Give the extent of all Plasmodium vivax-infected red blood cells.
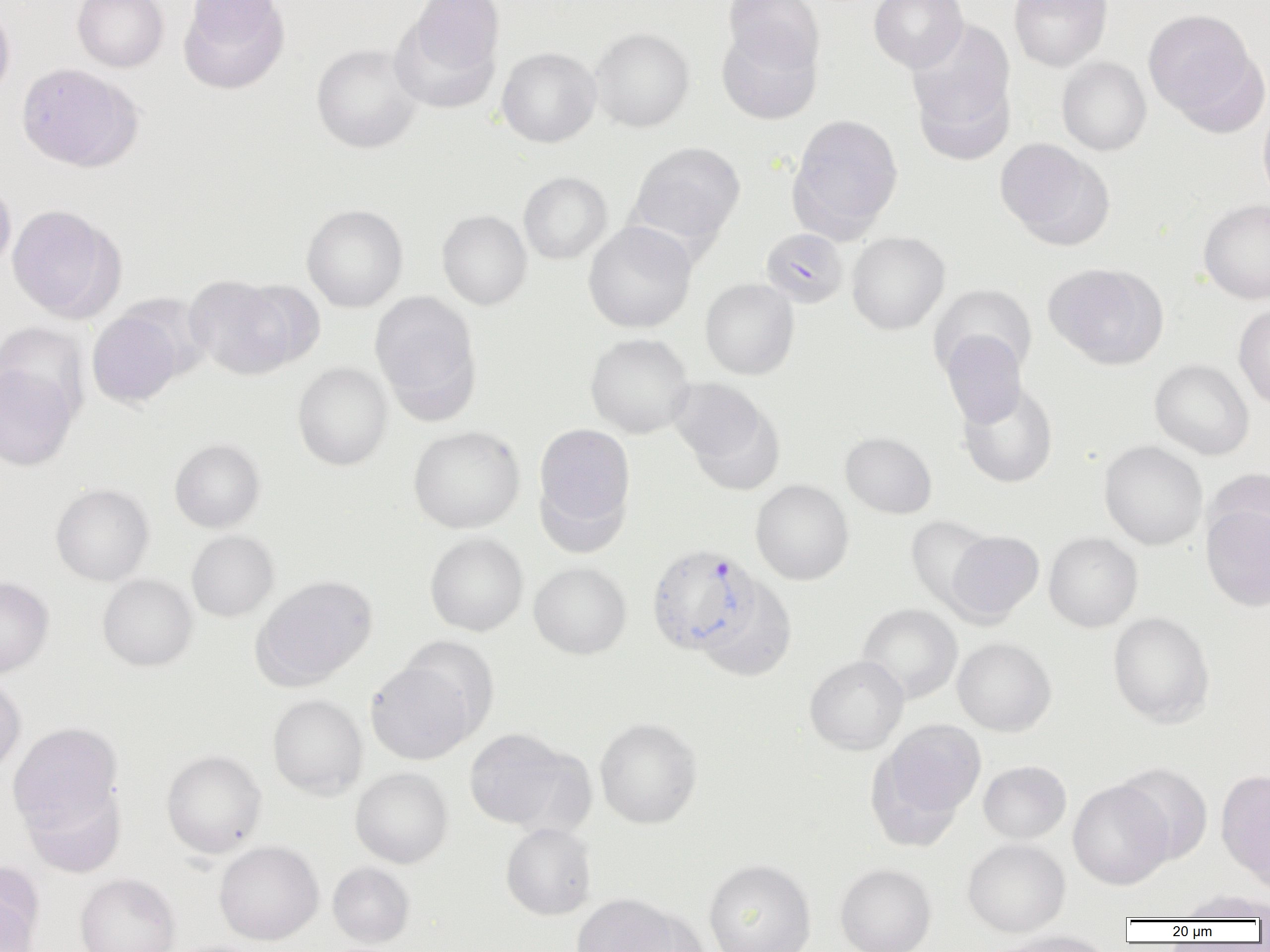

Approximate bounding boxes as [x1, y1, x2, y2] in pixels.
Plasmodium vivax-infected red blood cells: [646, 544, 761, 655].

Summary:
  - Uninfected red blood cell locations: [72, 0, 169, 72], [178, 0, 289, 93], [395, 0, 505, 95], [722, 0, 823, 72], [868, 0, 967, 72], [1009, 0, 1112, 71], [0, 3, 16, 102], [1143, 10, 1259, 124], [906, 20, 1016, 154], [716, 25, 823, 125], [591, 27, 694, 132], [311, 43, 423, 153], [496, 46, 602, 147], [1057, 57, 1152, 156], [16, 63, 141, 171], [1258, 104, 1270, 207], [788, 113, 903, 239], [995, 138, 1111, 247], [627, 141, 745, 250], [518, 171, 612, 264], [0, 180, 16, 276], [1198, 199, 1270, 304], [302, 204, 408, 312], [7, 205, 122, 321], [437, 209, 532, 310], [583, 221, 697, 333], [761, 227, 849, 308], [846, 231, 950, 335], [1043, 262, 1168, 369], [185, 274, 298, 380], [237, 278, 325, 369], [700, 278, 799, 380], [929, 284, 1036, 383], [369, 291, 481, 415], [1234, 304, 1270, 410], [87, 310, 183, 407], [0, 321, 90, 423], [585, 332, 694, 438], [941, 332, 1027, 427], [1149, 359, 1254, 460], [292, 362, 392, 470], [0, 363, 79, 470], [669, 379, 784, 494], [957, 380, 1058, 488], [533, 422, 636, 540], [408, 425, 525, 533], [840, 431, 937, 518], [169, 438, 265, 532], [1099, 440, 1208, 550], [1205, 468, 1270, 561], [750, 479, 854, 585], [50, 483, 154, 586], [1201, 502, 1270, 611], [907, 517, 996, 611], [186, 530, 279, 621], [946, 530, 1044, 624], [1044, 532, 1143, 632], [425, 533, 528, 636], [529, 562, 632, 658], [97, 574, 198, 671], [252, 575, 378, 689], [0, 577, 54, 677], [697, 580, 797, 681], [857, 603, 962, 703], [1107, 611, 1215, 727], [401, 636, 499, 736], [952, 637, 1056, 736], [804, 655, 909, 754], [366, 660, 476, 765], [0, 675, 25, 775], [267, 694, 368, 799], [595, 718, 702, 828], [872, 718, 986, 834], [8, 723, 122, 833], [463, 728, 573, 830], [161, 749, 267, 858], [978, 760, 1072, 844], [1114, 762, 1213, 864], [350, 767, 453, 868], [1216, 768, 1270, 886], [1068, 780, 1173, 890], [21, 783, 126, 877], [501, 822, 597, 920], [962, 838, 1071, 937], [214, 841, 324, 944], [703, 859, 817, 952], [0, 861, 44, 950], [328, 862, 415, 948], [835, 863, 937, 952], [75, 873, 181, 952], [1177, 889, 1270, 922], [572, 893, 684, 952], [625, 908, 711, 952], [984, 930, 1118, 952]
  - Slide-level diagnosis: Plasmodium vivax
  - Modality: light microscopy
  - Preparation: thin blood film
  - Image size: 1270×952 pixels
  - Field of view: single
  - Magnification: 1000x